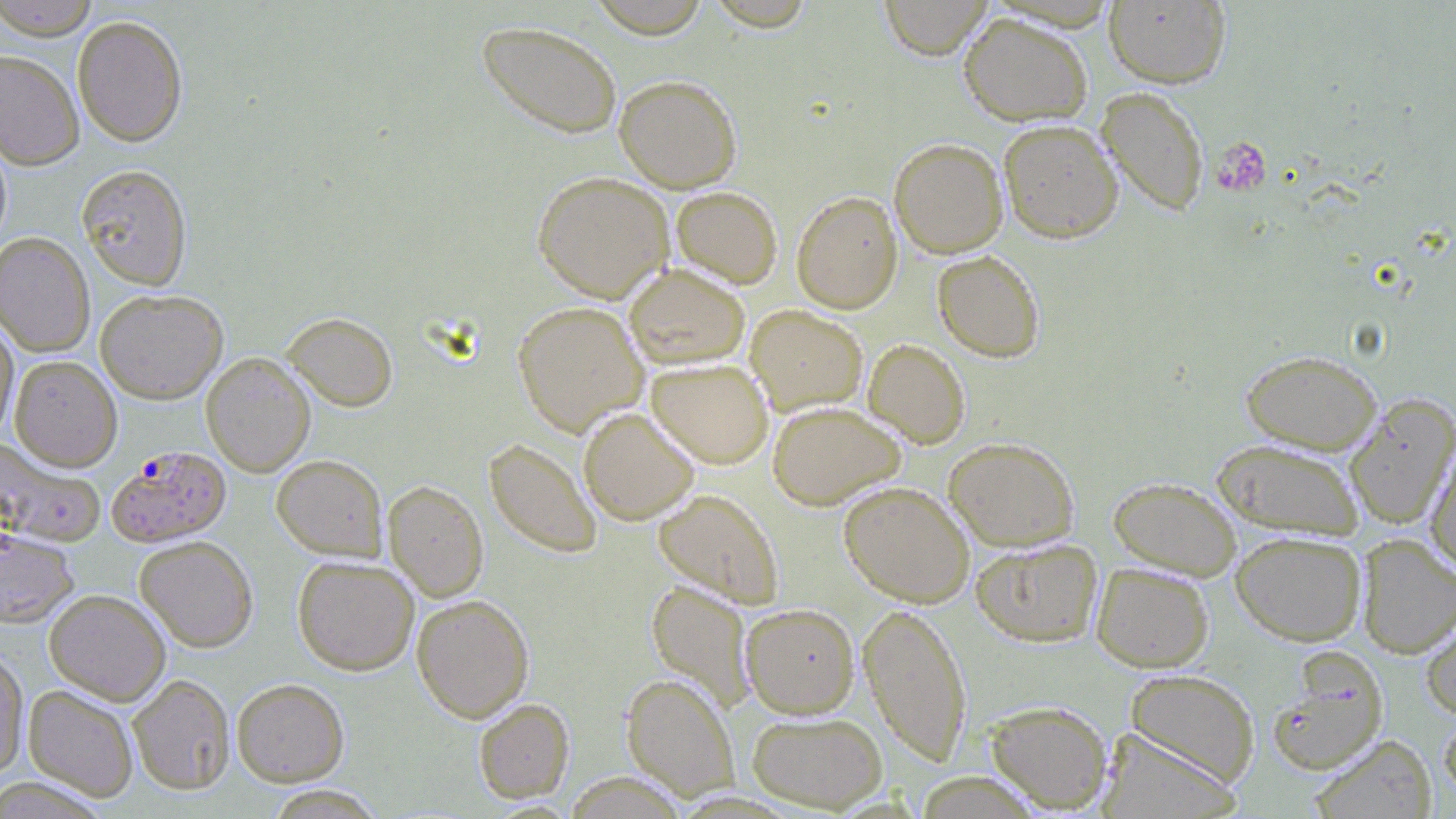
slide-level diagnosis = Plasmodium falciparum
platelet locations = approximate bounding boxes as (x1, y1, x2, y2) in pixels: (1212, 136, 1272, 196)
Plasmodium falciparum-infected red blood cell locations = approximate bounding boxes as (x1, y1, x2, y2) in pixels: (106, 445, 231, 547), (1267, 650, 1388, 776)
uninfected red blood cell locations = approximate bounding boxes as (x1, y1, x2, y2) in pixels: (0, 0, 99, 40), (586, 0, 712, 38), (878, 0, 994, 60), (1104, 1, 1231, 89), (703, 2, 818, 31), (958, 12, 1093, 127), (72, 15, 188, 147), (476, 19, 623, 139), (0, 50, 84, 170), (614, 74, 742, 193), (1096, 87, 1209, 217), (998, 118, 1123, 244), (0, 130, 12, 254), (889, 138, 1008, 259), (76, 164, 193, 289), (532, 170, 674, 303), (671, 186, 783, 289), (791, 190, 903, 313), (0, 232, 95, 357), (932, 250, 1045, 362), (623, 262, 750, 369), (95, 289, 228, 404), (512, 301, 648, 436), (745, 305, 868, 416), (281, 311, 398, 412), (0, 316, 18, 444), (863, 338, 970, 448), (1240, 349, 1382, 455), (201, 352, 316, 477), (10, 355, 122, 471), (647, 359, 773, 469), (1344, 393, 1456, 529), (767, 400, 906, 510), (578, 407, 700, 525), (944, 437, 1080, 552), (484, 438, 602, 558), (1212, 438, 1365, 539), (0, 439, 105, 547), (1424, 440, 1456, 576), (272, 454, 387, 560), (1108, 476, 1242, 579), (383, 479, 488, 602), (838, 481, 975, 607), (653, 489, 783, 609), (0, 528, 79, 628), (1231, 531, 1366, 646), (1356, 535, 1456, 658), (134, 536, 258, 652), (970, 538, 1103, 647), (293, 556, 419, 675), (1091, 562, 1214, 673), (646, 579, 756, 713), (44, 589, 170, 705), (411, 594, 534, 722), (859, 601, 972, 766), (740, 603, 860, 719), (1420, 603, 1456, 721), (0, 648, 29, 778), (1125, 669, 1260, 787), (622, 673, 739, 800), (128, 674, 235, 794), (231, 677, 349, 786), (24, 685, 138, 801), (473, 698, 574, 803), (984, 699, 1113, 813), (1438, 709, 1456, 804), (746, 710, 888, 813), (1095, 727, 1241, 819), (1311, 734, 1437, 819)
magnification = 1000x
field of view = single
preparation = thin blood film
stain = May-Grünwald-Giemsa
image size = 1456×819 pixels
modality = light microscopy